Report the malaria status of this cell.
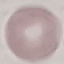

Uninfected.

Summary:
  - Image type: automatically extracted cell patch, resized to 64 × 64 pixels
  - Preparation: thin blood film
  - Capture: smartphone through the microscope eyepiece
  - Stain: Giemsa